Assess this cell for malaria.
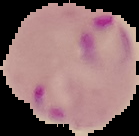

Parasitized.

image_type: segmented cell region on a black background
image_size: 139×136 pixels
preparation: thin blood smear